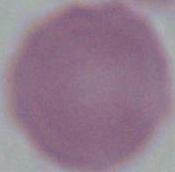
identification = erythrocyte
modality = micrograph
magnification = 1000x